Comment on the morphology of the erythrocytes.
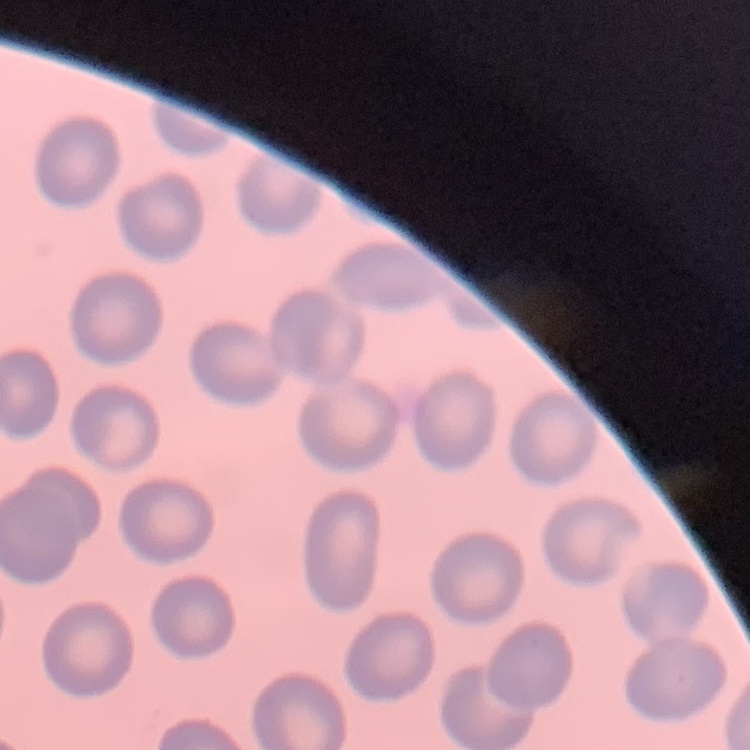
They show no rouleaux formation.

Thin blood smear. One tile cut from a larger photomicrograph. Field's or Giemsa stain.